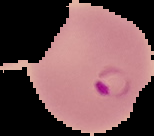
image type = segmented cell region on a black background
preparation = thin blood film
image size = 154×136 pixels
result = Plasmodium parasites identified